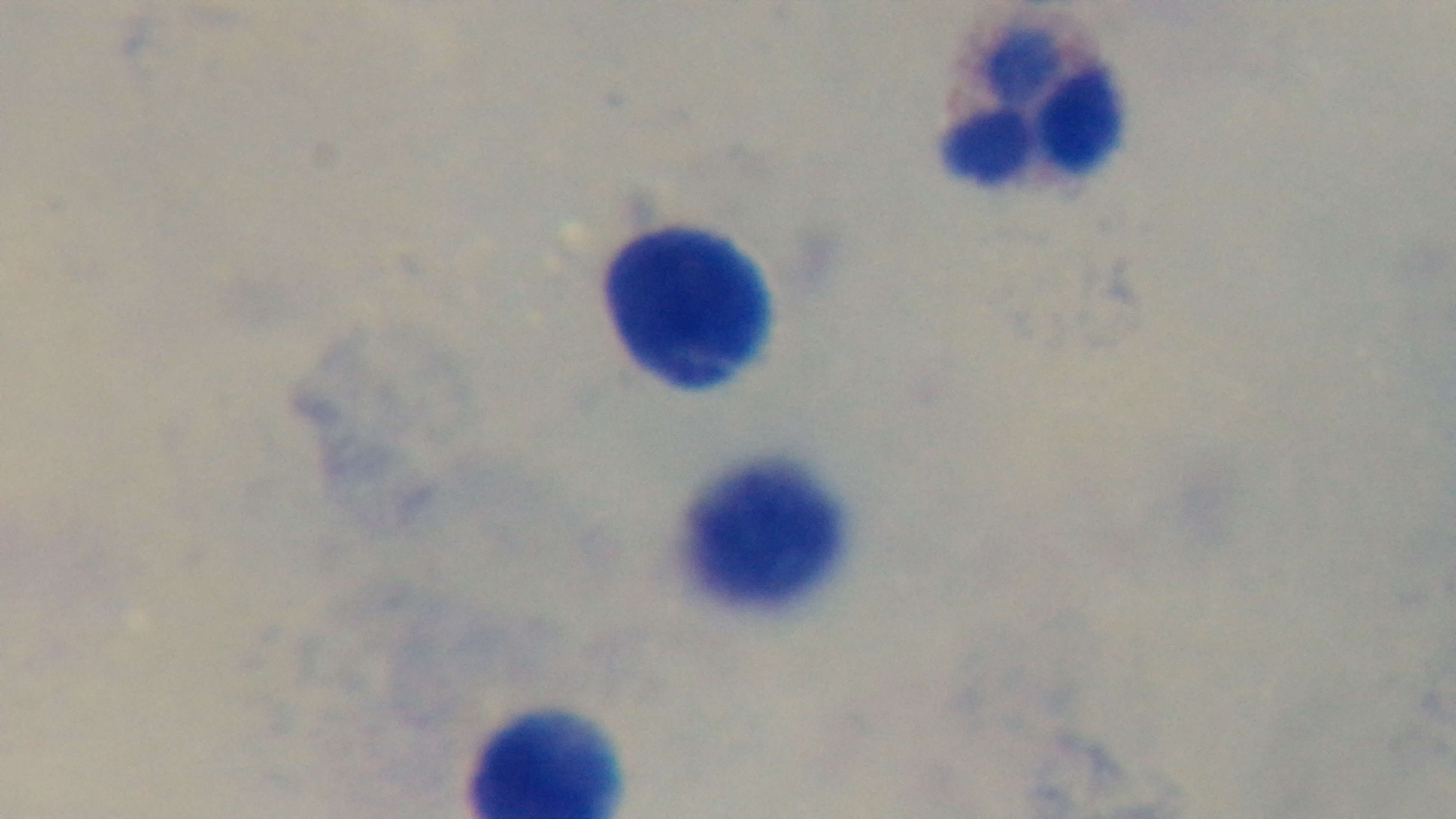
field of view = single
stain = Giemsa
capture = mounted 4K digital camera
preparation = thick
modality = light microscopy
malaria status = negative
objective = 100x oil immersion